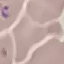 Malaria status: parasitized. Thin blood film. Acquired by smartphone through the microscope eyepiece. Cell patch, automatically extracted from a larger field of view and resized to 64 × 64 pixels. Giemsa-stained preparation.